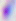

Summary:
  - Modality: micrograph
  - Identification: Toxoplasma gondii
  - Magnification: 400x